Name the parasite shown.
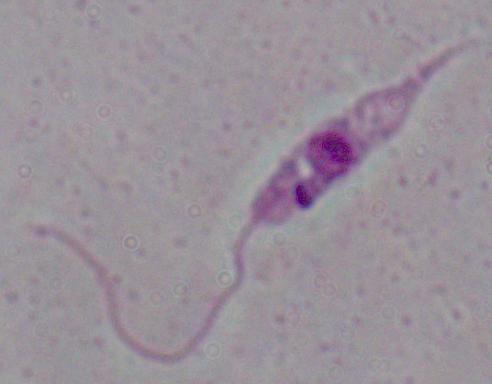

Leishmania.

Micrograph. Captured at 1000x magnification.